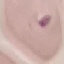

malaria status = uninfected
image type = cell patch, automatically extracted from a larger field of view and resized to 64 × 64 pixels
stain = Giemsa
preparation = thin blood smear
capture = smartphone through the microscope eyepiece